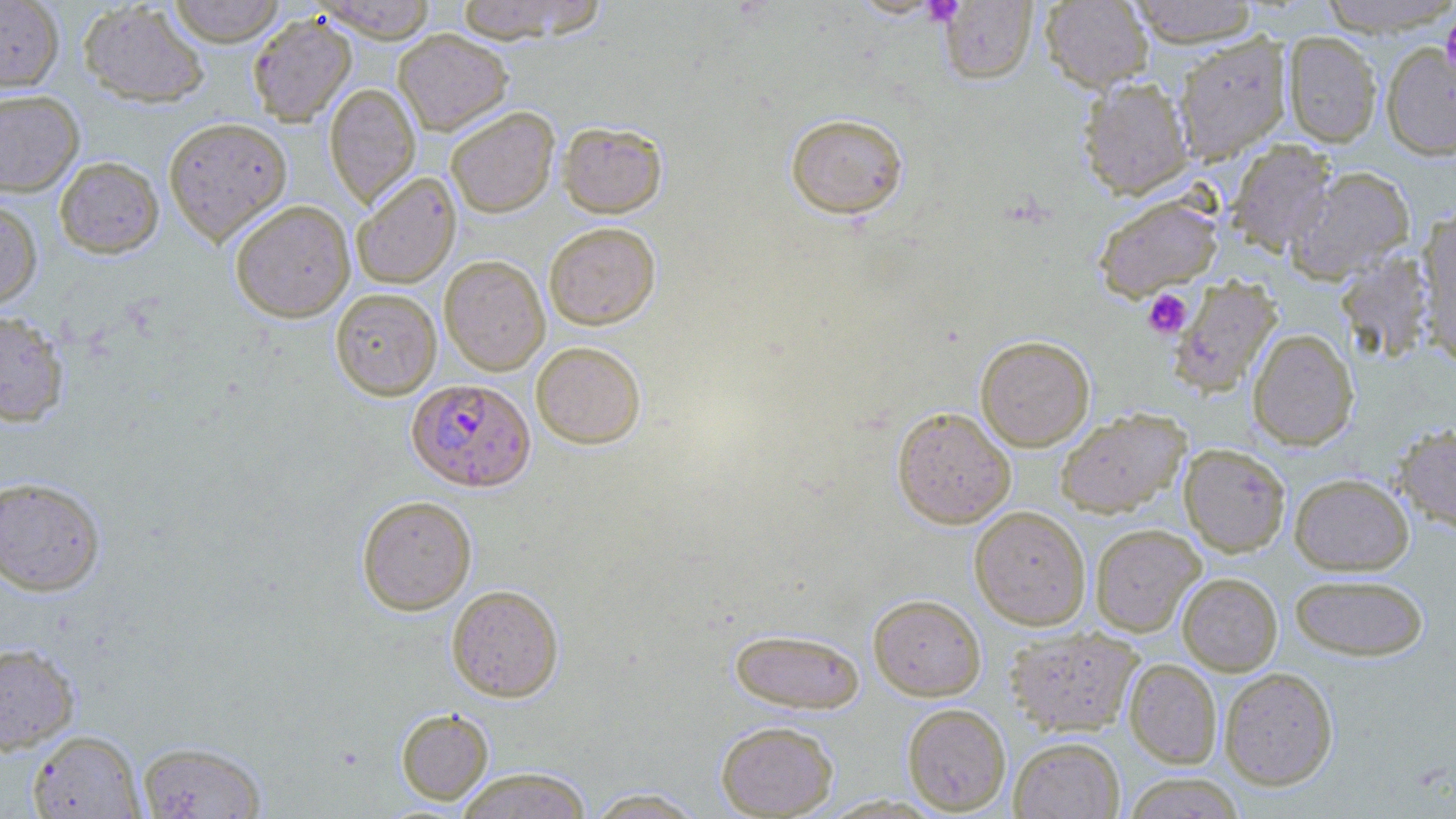 Approximate bounding boxes as (x1, y1, x2, y2) in pixels. Uninfected red blood cell locations: (0, 0, 64, 92), (168, 0, 287, 46), (313, 0, 438, 42), (453, 0, 606, 43), (1041, 0, 1153, 93), (1128, 0, 1260, 46), (1316, 0, 1456, 35), (78, 1, 210, 108), (939, 1, 1037, 84), (247, 13, 357, 126), (393, 29, 512, 135), (1282, 31, 1383, 147), (1173, 34, 1292, 162), (1380, 40, 1456, 160), (1078, 77, 1194, 199), (324, 83, 420, 209), (0, 90, 84, 197), (445, 106, 559, 217), (785, 112, 909, 219), (163, 116, 292, 246), (558, 120, 668, 218), (1227, 140, 1335, 254), (54, 156, 164, 259), (1288, 165, 1415, 283), (351, 171, 461, 289), (1093, 194, 1223, 300), (0, 199, 43, 310), (229, 199, 355, 322), (1417, 206, 1456, 362), (544, 222, 660, 329), (1336, 251, 1437, 364), (439, 255, 550, 375), (1169, 275, 1283, 397), (330, 288, 442, 400), (0, 310, 69, 427), (1248, 328, 1358, 450), (975, 335, 1094, 451), (531, 341, 646, 449), (892, 406, 1016, 528), (1056, 408, 1190, 517), (1393, 424, 1456, 536), (1179, 443, 1290, 556), (1289, 472, 1414, 575), (0, 476, 106, 596), (357, 495, 477, 615), (970, 506, 1091, 629), (1090, 523, 1205, 636), (1177, 572, 1282, 675), (1290, 573, 1429, 660), (446, 584, 564, 702), (868, 593, 986, 700), (1003, 625, 1143, 737), (729, 627, 865, 713), (0, 642, 80, 754), (1124, 659, 1222, 768), (1220, 667, 1338, 790), (902, 703, 1011, 815), (396, 708, 494, 804), (716, 720, 839, 818), (27, 730, 145, 818), (1010, 737, 1124, 818), (137, 740, 267, 818), (454, 767, 593, 819), (1122, 773, 1246, 818), (584, 787, 707, 818). Plasmodium falciparum-infected red blood cell locations: (407, 377, 536, 492). Platelet locations: (1440, 12, 1456, 77), (1142, 289, 1192, 338). Slide-level diagnosis: Plasmodium falciparum. Single field of view. Thin blood film. Image is 1456×819 pixels. Light microscopy. Captured at 1000x magnification. May-Grünwald-Giemsa-stained preparation.